Report the malaria status of this cell.
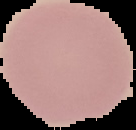
Uninfected.

Image is 136×130 pixels. Cell region segmented out of the field of view; the surrounding area is masked to black. From a thin blood film.